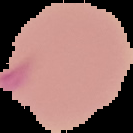
Summary:
  - Malaria status: parasitized
  - Image type: segmented cell region on a black background
  - Preparation: thin blood film
  - Image size: 133×133 pixels